Assess this cell for malaria.
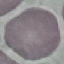
It is uninfected.

capture = smartphone through the microscope eyepiece
stain = Giemsa
image type = cell patch, automatically extracted from a larger field of view and resized to 64 × 64 pixels
preparation = thin blood smear